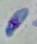

Summary:
  - Identification: Toxoplasma gondii
  - Magnification: 1000x
  - Modality: photomicrograph